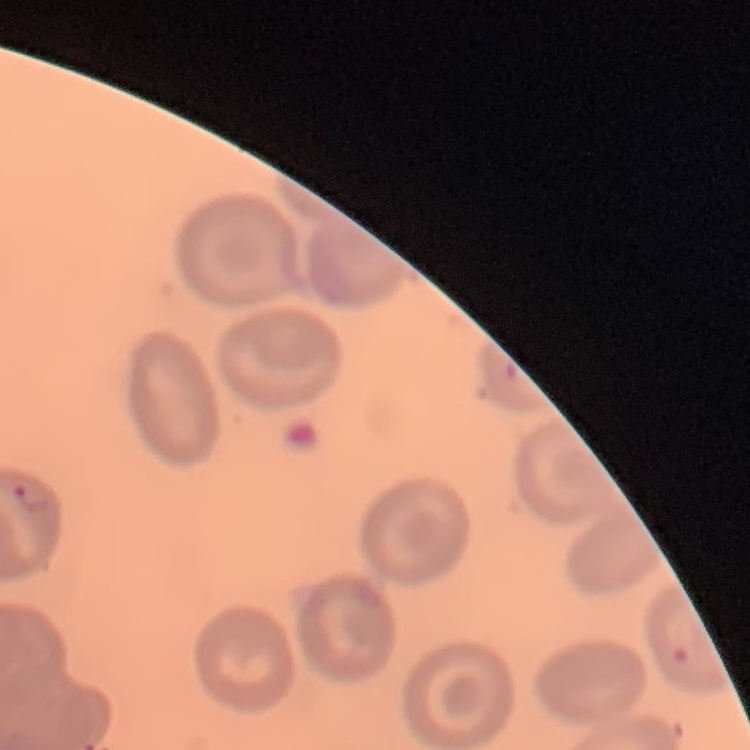 The erythrocytes show no rouleaux formation. Square crop of a larger photomicrograph. Thin blood smear. Stained with either Field's or Giemsa.